Outline each blood parasite and name the species.
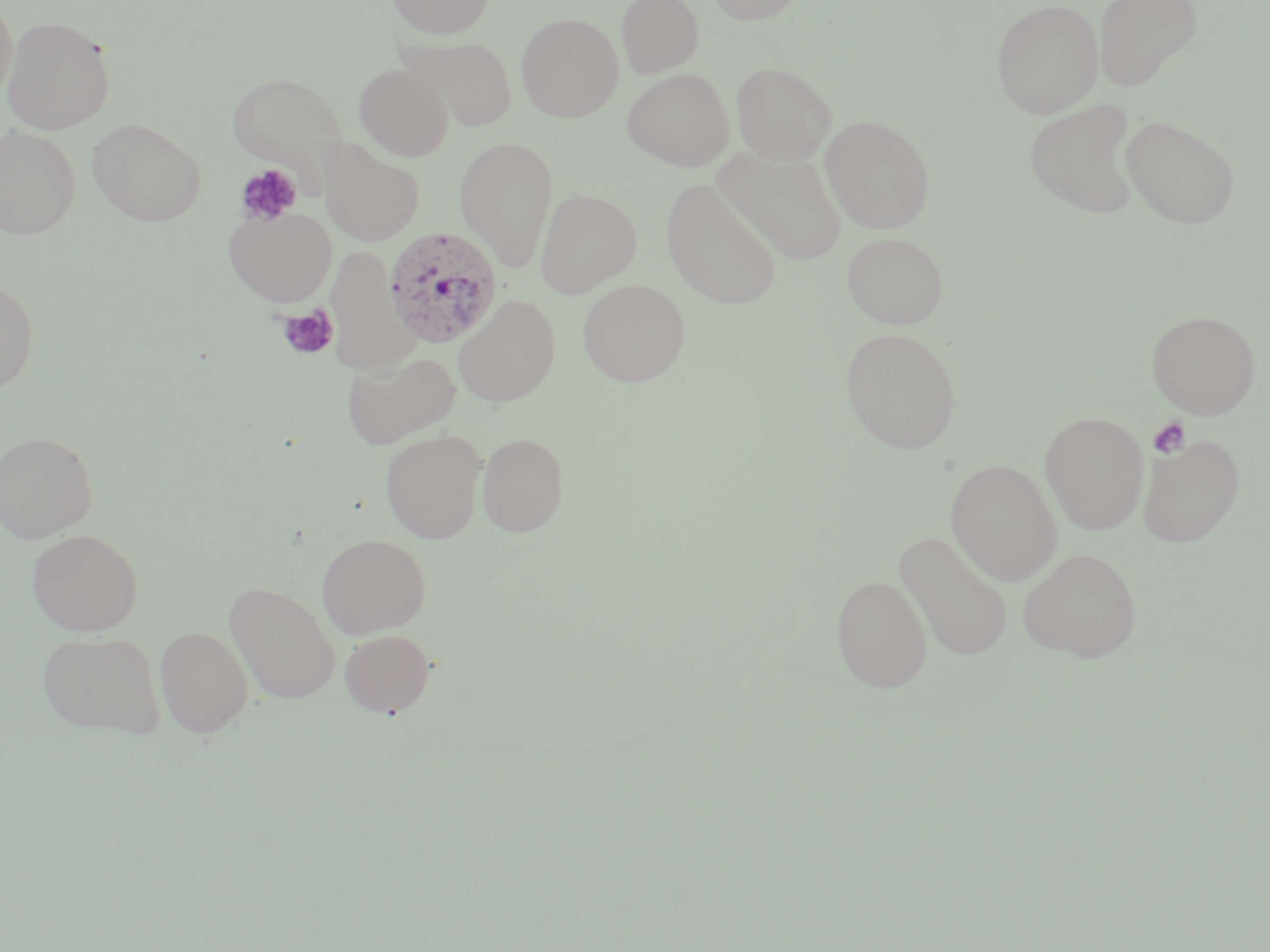
Approximate bounding boxes as (x1, y1, x2, y2) in pixels.
Plasmodium vivax-infected red blood cells: (383, 226, 504, 348).
No Plasmodium falciparum, Plasmodium ovale, Plasmodium malariae, Babesia divergens, or Trypanosoma brucei observed.

Platelet locations: (234, 164, 302, 226), (277, 305, 338, 361), (1148, 417, 1191, 459). Uninfected red blood cell locations: (0, 0, 17, 102), (387, 0, 494, 39), (616, 0, 704, 78), (704, 0, 808, 24), (991, 0, 1104, 118), (1093, 0, 1202, 90), (516, 12, 623, 122), (2, 15, 116, 134), (406, 36, 518, 131), (731, 61, 837, 164), (355, 63, 454, 161), (622, 68, 734, 171), (228, 72, 347, 173), (1025, 99, 1143, 218), (820, 114, 936, 233), (1120, 115, 1239, 228), (87, 118, 207, 226), (0, 126, 82, 238), (454, 136, 559, 272), (320, 139, 425, 245), (715, 146, 848, 265), (661, 178, 782, 310), (536, 188, 642, 297), (224, 205, 337, 306), (841, 231, 949, 329), (326, 249, 417, 375), (577, 278, 691, 387), (0, 280, 39, 392), (454, 294, 560, 407), (1146, 310, 1261, 418), (840, 326, 962, 454), (342, 350, 461, 448), (1039, 411, 1149, 534), (0, 430, 99, 542), (380, 430, 486, 543), (476, 431, 570, 537), (1138, 434, 1243, 547), (945, 459, 1062, 585), (26, 527, 144, 635), (894, 531, 1015, 662), (317, 533, 432, 638), (1018, 547, 1142, 661), (830, 574, 933, 692), (225, 580, 342, 704), (154, 626, 254, 737), (340, 628, 436, 717), (36, 630, 168, 739). Slide-level diagnosis: Plasmodium vivax. Optical microscopy. Thin blood smear. Image is 1270×952 pixels. 1000x magnification. May-Grünwald-Giemsa stain. Single field of view.